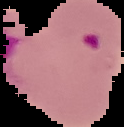
Summary:
  - Image type: segmented cell region with the area outside set to black
  - Result: malaria parasites detected
  - Image size: 124×127 pixels
  - Preparation: thin blood film